Locate every blood parasite and identify its species.
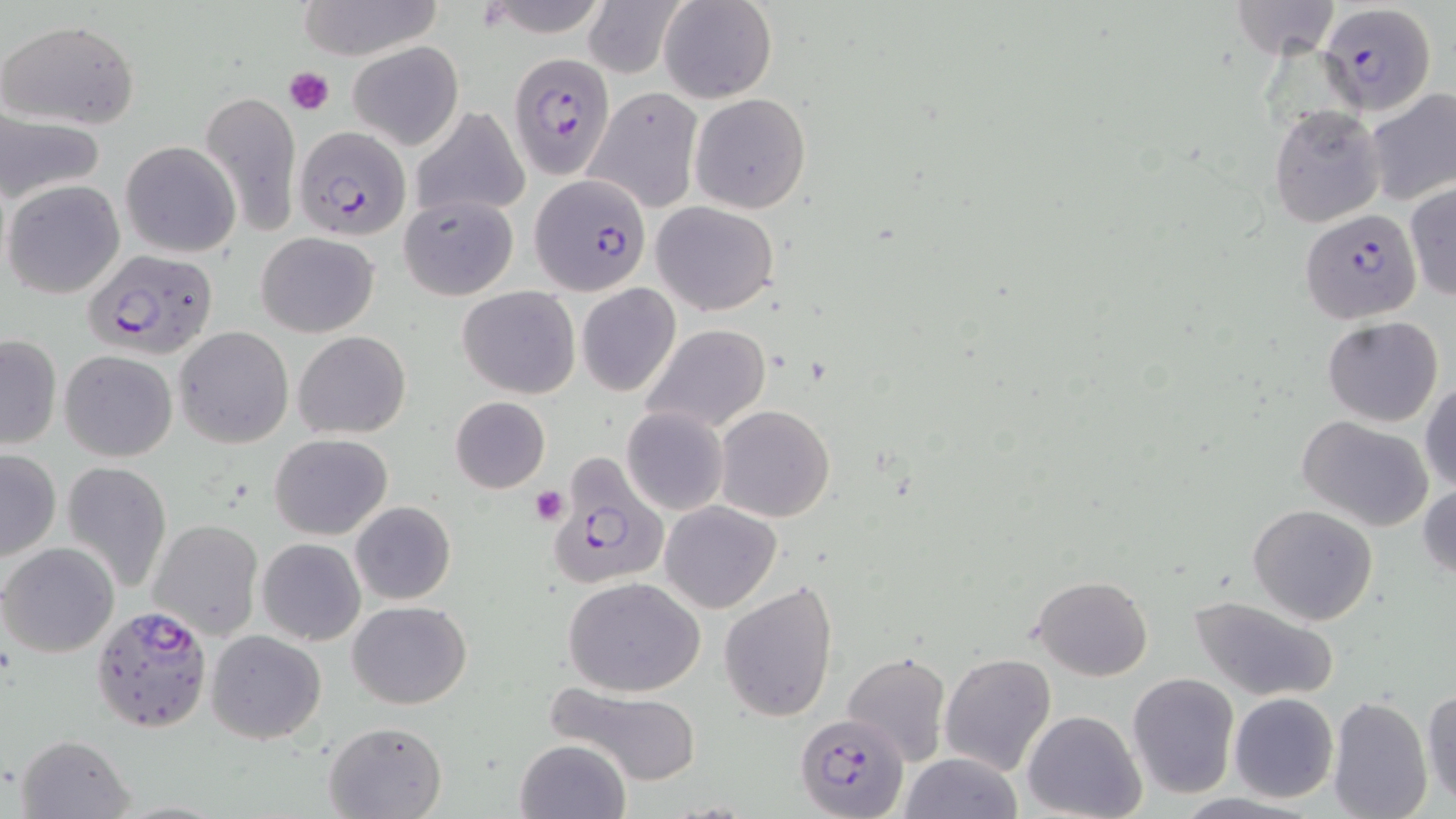
Approximate bounding boxes as [x1, y1, x2, y2] in pixels.
Plasmodium falciparum-infected red blood cells: [1318, 2, 1437, 116], [506, 54, 617, 179], [294, 126, 413, 242], [531, 173, 653, 295], [1298, 208, 1421, 322], [85, 250, 220, 358], [546, 459, 668, 589], [92, 604, 214, 734], [796, 714, 907, 818].
No Plasmodium ovale, Plasmodium malariae, Plasmodium vivax, Babesia divergens, or Trypanosoma brucei observed.

slide_level_diagnosis: Plasmodium falciparum
field_of_view: one of a larger specimen
modality: optical microscopy
magnification: 1000x
image_size: 1456×819 pixels
stain: May-Grünwald-Giemsa
platelet_locations: 'approximate bounding boxes as [x1, y1, x2, y2] in pixels: [284, 67, 334, 116], [528, 483, 570, 524]'
uninfected_red_blood_cell_locations: 'approximate bounding boxes as [x1, y1, x2, y2] in pixels: [583, 0, 685, 78], [658, 0, 777, 104], [295, 1, 443, 60], [1229, 1, 1341, 61], [0, 18, 140, 129], [347, 41, 464, 151], [585, 85, 704, 214], [1363, 87, 1456, 205], [200, 90, 302, 236], [690, 92, 811, 213], [1268, 104, 1384, 228], [408, 106, 532, 220], [1, 112, 105, 205], [120, 140, 241, 258], [4, 181, 125, 299], [1405, 183, 1455, 302], [399, 196, 517, 300], [651, 201, 780, 315], [255, 232, 380, 338], [577, 283, 679, 396], [458, 284, 580, 398], [1321, 316, 1446, 425], [643, 324, 771, 433], [173, 325, 293, 449], [293, 330, 411, 441], [1, 334, 62, 450], [60, 349, 176, 461], [1420, 380, 1456, 492], [449, 396, 550, 494], [714, 405, 835, 521], [621, 406, 728, 515], [1297, 417, 1434, 533], [270, 432, 393, 540], [1, 449, 61, 562], [65, 464, 169, 594], [1418, 481, 1456, 585], [351, 501, 456, 604], [660, 501, 781, 613], [1248, 504, 1379, 625], [147, 519, 263, 641], [256, 538, 365, 645], [0, 542, 119, 658], [564, 576, 705, 697], [1032, 576, 1154, 678], [719, 581, 837, 724], [1189, 595, 1341, 703], [347, 600, 471, 709], [206, 630, 326, 743], [843, 651, 950, 765], [939, 652, 1055, 776], [1127, 673, 1239, 798], [551, 680, 702, 785], [1422, 686, 1456, 805], [1228, 692, 1338, 804], [1327, 695, 1432, 819], [1022, 709, 1146, 819], [324, 720, 448, 819], [15, 733, 135, 819], [515, 738, 629, 818], [899, 752, 1023, 819]'
preparation: thin blood film